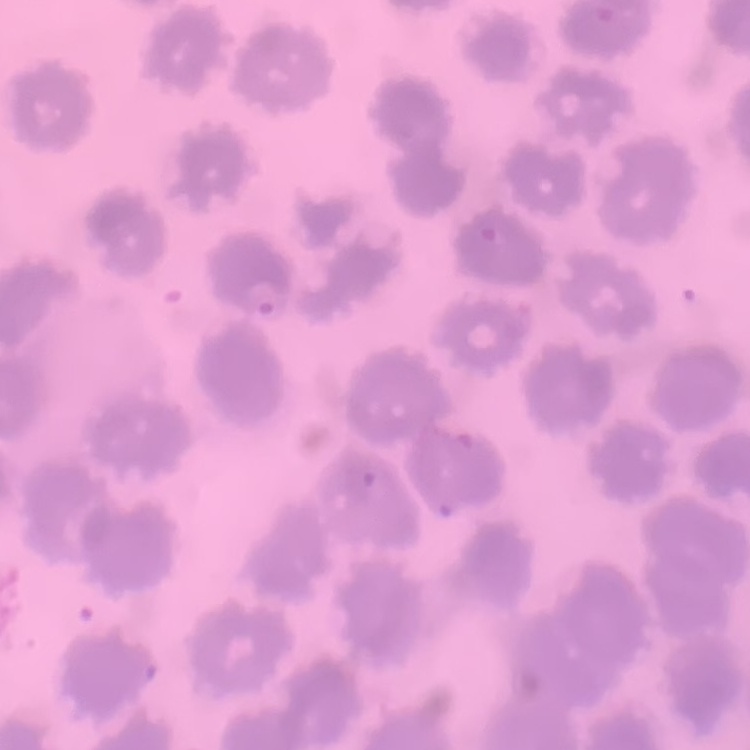

Summary:
  - Red blood cell morphology: no rouleaux formation
  - Preparation: thin blood film
  - Stain: Field's or Giemsa
  - Image type: one tile cut from a larger photomicrograph